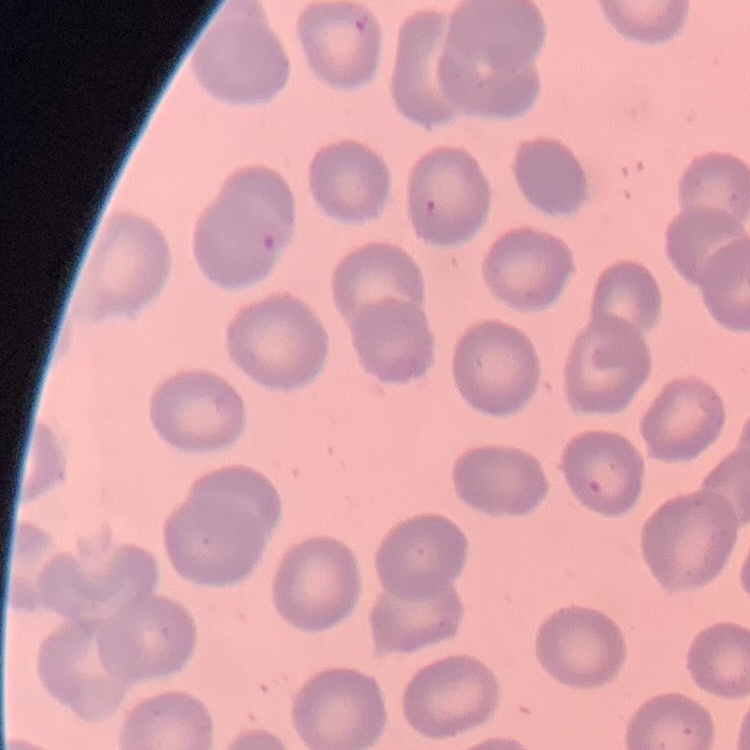

red_blood_cell_morphology: no rouleaux formation
image_type: square crop of a larger photomicrograph
preparation: thin blood smear
stain: Field's or Giemsa